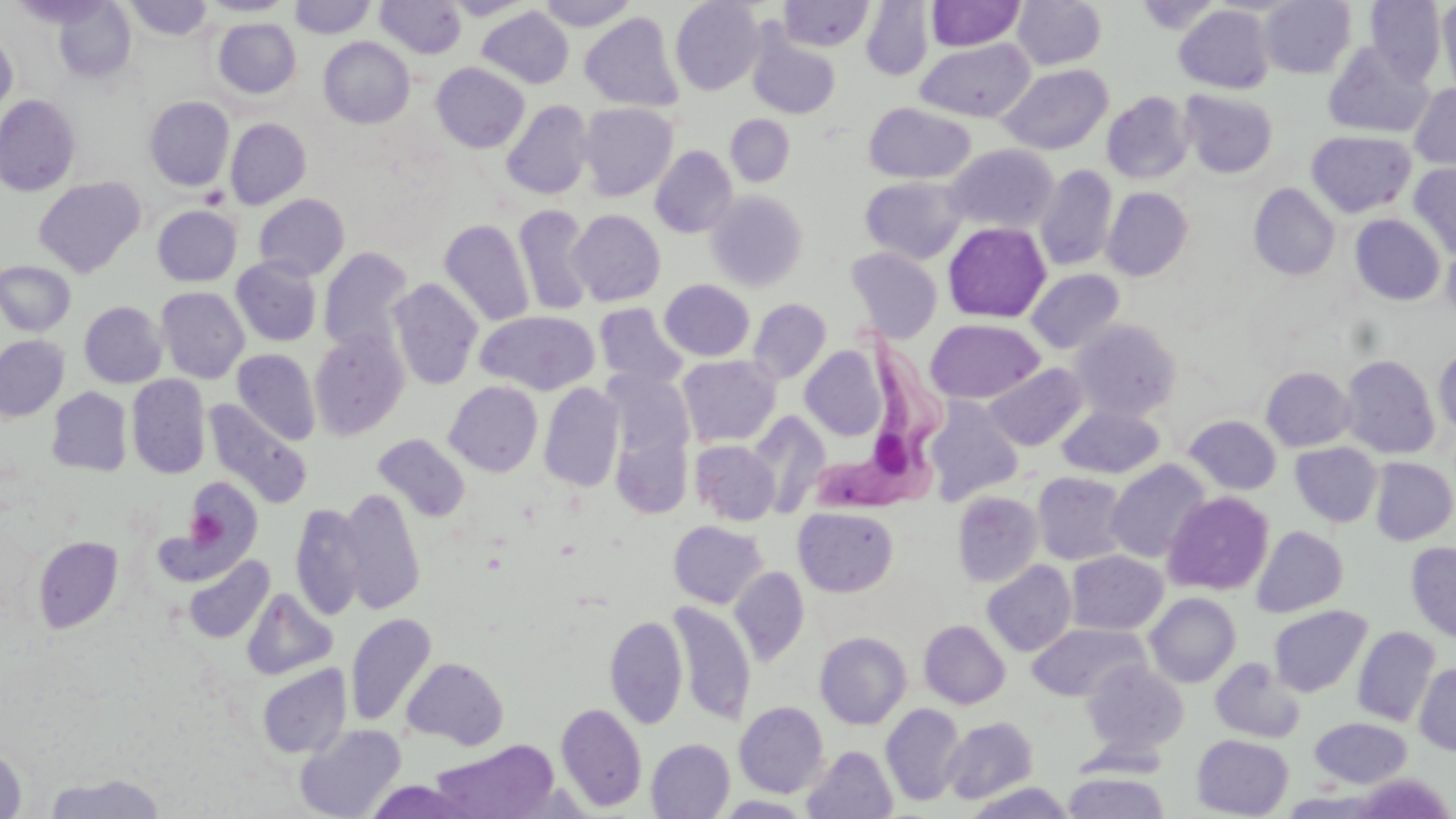
slide-level diagnosis = Trypanosoma brucei
preparation = thin blood film
uninfected red blood cell locations = approximate bounding boxes as (x1, y1, x2, y2) in pixels: (124, 0, 213, 42), (200, 0, 295, 16), (290, 0, 375, 38), (377, 0, 466, 59), (445, 0, 531, 19), (535, 0, 637, 30), (1013, 0, 1107, 70), (1260, 0, 1356, 78), (1366, 0, 1447, 85), (670, 1, 765, 95), (779, 1, 874, 52), (861, 1, 933, 80), (926, 1, 1025, 50), (1136, 1, 1221, 33), (53, 2, 137, 82), (1438, 2, 1456, 97), (1175, 5, 1274, 93), (477, 7, 574, 89), (580, 12, 683, 112), (213, 18, 301, 98), (747, 27, 841, 119), (0, 34, 17, 115), (319, 37, 414, 128), (916, 38, 1034, 122), (1323, 42, 1434, 138), (431, 62, 530, 153), (998, 64, 1113, 155), (1410, 84, 1456, 171), (1180, 90, 1278, 178), (1102, 91, 1195, 184), (0, 94, 81, 197), (144, 96, 235, 190), (502, 100, 594, 200), (578, 103, 677, 201), (864, 103, 976, 184), (726, 114, 795, 186), (225, 118, 311, 209), (1307, 130, 1416, 218), (944, 144, 1058, 234), (650, 145, 738, 238), (1408, 163, 1456, 258), (1035, 165, 1118, 271), (860, 175, 967, 264), (33, 177, 145, 277), (1248, 183, 1340, 281), (1102, 187, 1193, 281), (706, 190, 808, 292), (253, 193, 350, 281), (153, 205, 242, 286), (514, 205, 594, 316), (568, 210, 665, 306), (1350, 214, 1445, 305), (439, 219, 535, 328), (943, 221, 1051, 323), (1442, 242, 1456, 324), (319, 247, 414, 356), (846, 247, 943, 342), (231, 257, 322, 346), (0, 261, 75, 335), (1027, 269, 1124, 354), (388, 278, 483, 390), (659, 279, 754, 361), (156, 286, 249, 383), (748, 298, 831, 383), (79, 301, 167, 388), (594, 303, 689, 388), (475, 310, 599, 395), (925, 319, 1045, 404), (1070, 319, 1181, 421), (308, 330, 409, 440), (948, 334, 1080, 429), (0, 335, 69, 421), (1433, 345, 1456, 436), (801, 347, 887, 440), (233, 349, 321, 445), (677, 355, 781, 446), (1341, 355, 1440, 459), (984, 364, 1087, 451), (1261, 366, 1356, 451), (603, 371, 694, 461), (127, 374, 211, 479), (445, 381, 543, 477), (539, 382, 624, 492), (46, 387, 133, 476), (924, 397, 1024, 504), (204, 399, 313, 509), (1057, 403, 1164, 479), (748, 412, 831, 517), (1184, 415, 1281, 495), (612, 429, 693, 518), (373, 434, 470, 523), (691, 440, 780, 525), (1290, 442, 1382, 527), (1370, 457, 1456, 545), (1106, 459, 1211, 563), (1032, 471, 1130, 565), (180, 476, 262, 571), (339, 488, 425, 615), (951, 491, 1043, 587), (1163, 491, 1274, 595), (290, 503, 366, 620), (794, 506, 899, 596), (0, 518, 33, 615), (669, 520, 767, 608), (1252, 526, 1348, 617), (33, 536, 123, 632), (1406, 542, 1456, 643), (1066, 550, 1167, 635), (183, 555, 274, 644), (982, 560, 1077, 656), (730, 567, 809, 666), (242, 588, 338, 680), (1145, 593, 1241, 687), (668, 602, 756, 727), (1268, 605, 1371, 697), (345, 613, 436, 728), (605, 615, 688, 729), (919, 620, 1010, 709), (1027, 622, 1149, 702), (1352, 626, 1441, 726), (815, 631, 912, 729), (401, 657, 509, 750), (1210, 658, 1305, 743), (1082, 661, 1189, 757), (1414, 662, 1456, 756), (256, 664, 351, 759), (734, 702, 829, 798), (556, 703, 648, 811), (881, 704, 965, 806), (942, 716, 1038, 804), (1310, 717, 1412, 788), (294, 724, 407, 819), (1191, 734, 1294, 818), (646, 738, 735, 818), (431, 739, 559, 819), (0, 743, 28, 819), (803, 745, 897, 819), (1063, 771, 1170, 818), (42, 773, 166, 818), (1349, 774, 1454, 818), (363, 780, 476, 818), (965, 782, 1076, 818), (1279, 790, 1386, 818), (717, 795, 815, 818)
image size = 1456×819 pixels
field of view = single
magnification = 1000x
stain = May-Grünwald-Giemsa
platelet locations = approximate bounding boxes as (x1, y1, x2, y2) in pixels: (186, 507, 225, 548)
modality = optical microscopy
Trypanosoma brucei locations = approximate bounding boxes as (x1, y1, x2, y2) in pixels: (823, 328, 953, 519)